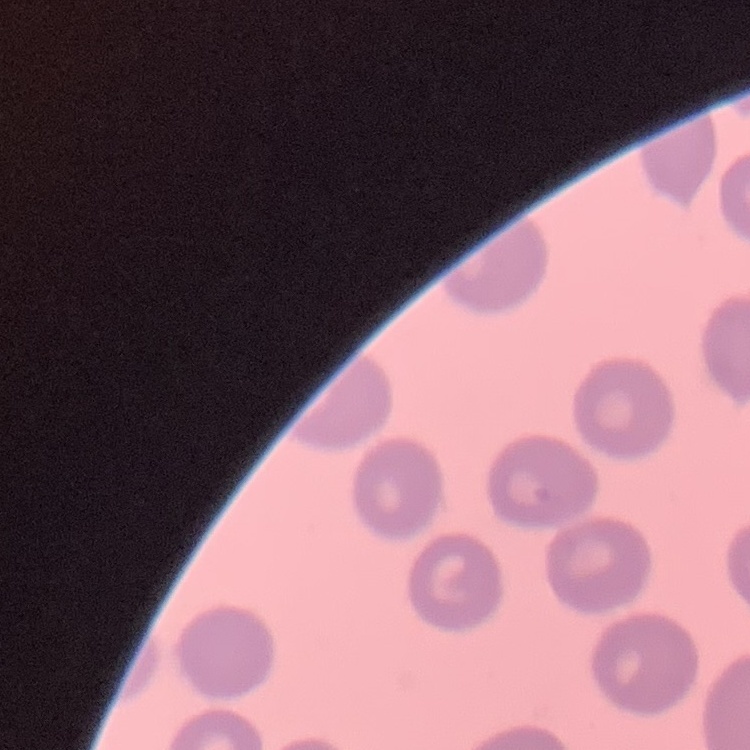
The red blood cells exhibit no rouleaux formation. Stained with either Field's or Giemsa. Square crop of a larger photomicrograph. Thin blood smear.